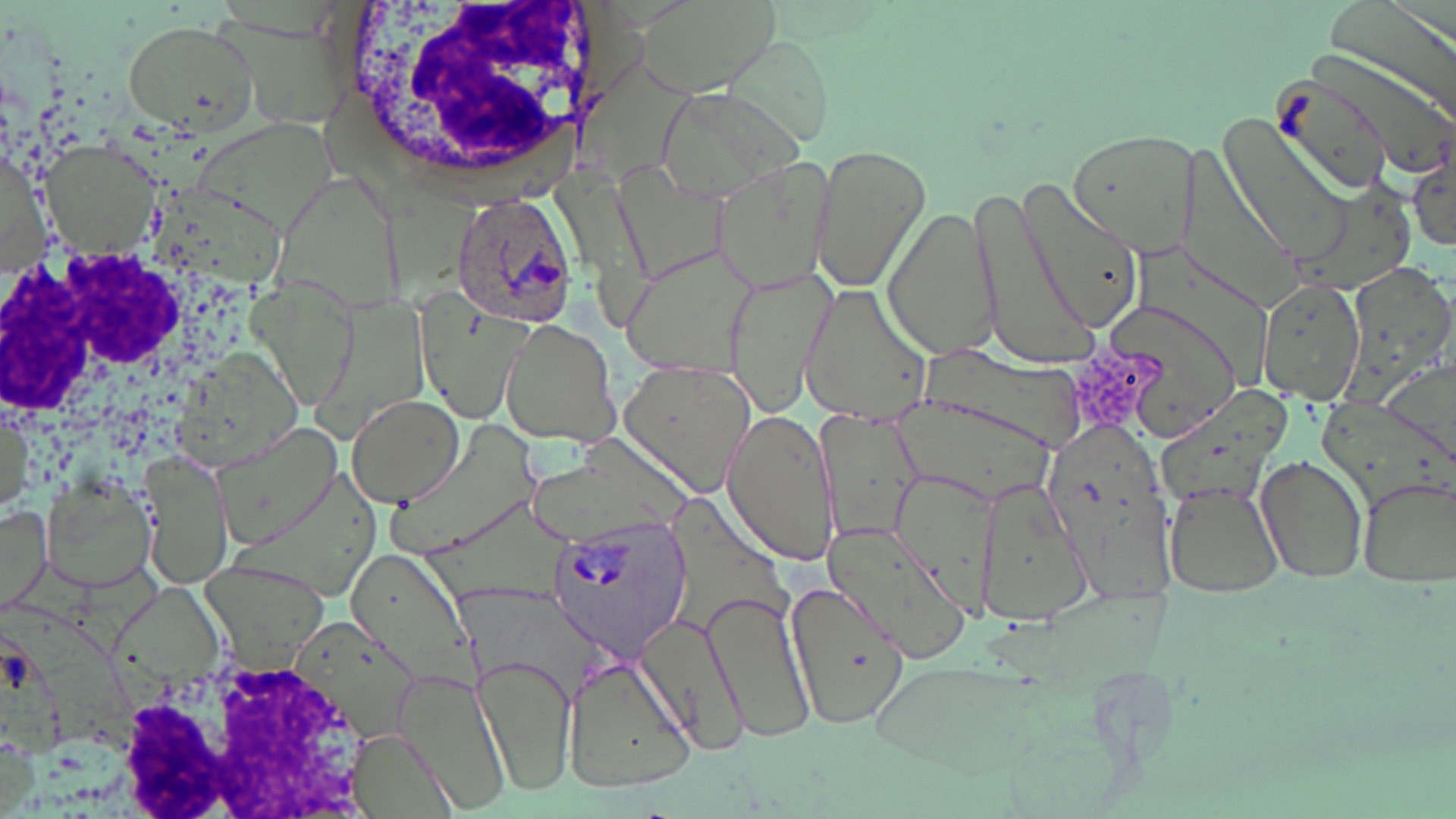
{
  "slide_level_diagnosis": "Plasmodium ovale",
  "magnification": "1000x",
  "stain": "May-Grünwald-Giemsa",
  "plasmodium_ovale_infected_red_blood_cell_locations": "approximate bounding boxes as (x1,y1)-(x2,y2) corner pairs in pixels: (450,189)-(581,325), (546,515)-(694,662)",
  "field_of_view": "one of a larger specimen",
  "white_blood_cell_locations": "approximate bounding boxes as (x1,y1)-(x2,y2) corner pairs in pixels: (317,0)-(628,195), (0,241)-(202,422), (105,659)-(374,817)",
  "modality": "light microscopy",
  "preparation": "thin blood smear",
  "image_size": "1456×819 pixels",
  "uninfected_red_blood_cell_locations": "approximate bounding boxes as (x1,y1)-(x2,y2) corner pairs in pixels: (118,17)-(261,137), (1265,59)-(1438,196), (652,86)-(805,206), (1215,112)-(1357,265), (1066,127)-(1205,256), (45,143)-(156,256), (806,143)-(932,297), (1408,151)-(1456,253), (710,158)-(840,296), (1013,173)-(1149,338), (968,180)-(1091,370), (884,201)-(999,364), (620,245)-(759,377), (723,265)-(835,415), (1257,275)-(1366,403), (797,282)-(935,425), (496,318)-(622,447), (617,361)-(755,500), (344,393)-(467,507), (0,400)-(38,520), (815,408)-(923,548), (721,410)-(839,566), (1039,412)-(1179,589), (212,422)-(344,551), (139,448)-(232,585), (1256,453)-(1369,584), (1356,472)-(1456,590), (38,477)-(155,595), (1161,479)-(1288,599), (979,482)-(1094,627), (0,503)-(49,618), (822,518)-(974,662), (344,541)-(478,692), (782,577)-(913,730), (702,589)-(818,743), (636,610)-(752,756), (290,616)-(422,746), (478,651)-(575,799), (562,653)-(696,796), (384,679)-(507,805), (348,728)-(462,818)"
}